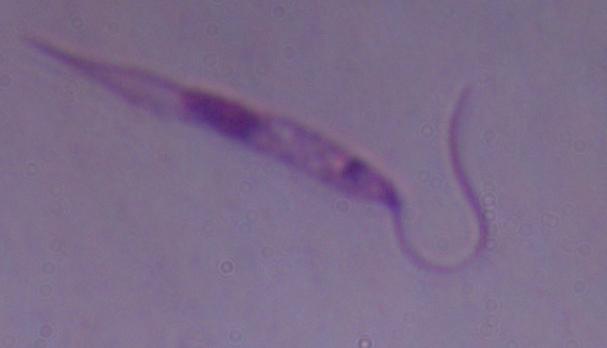

Summary:
  - Identification: Leishmania
  - Modality: photomicrograph
  - Magnification: 1000x